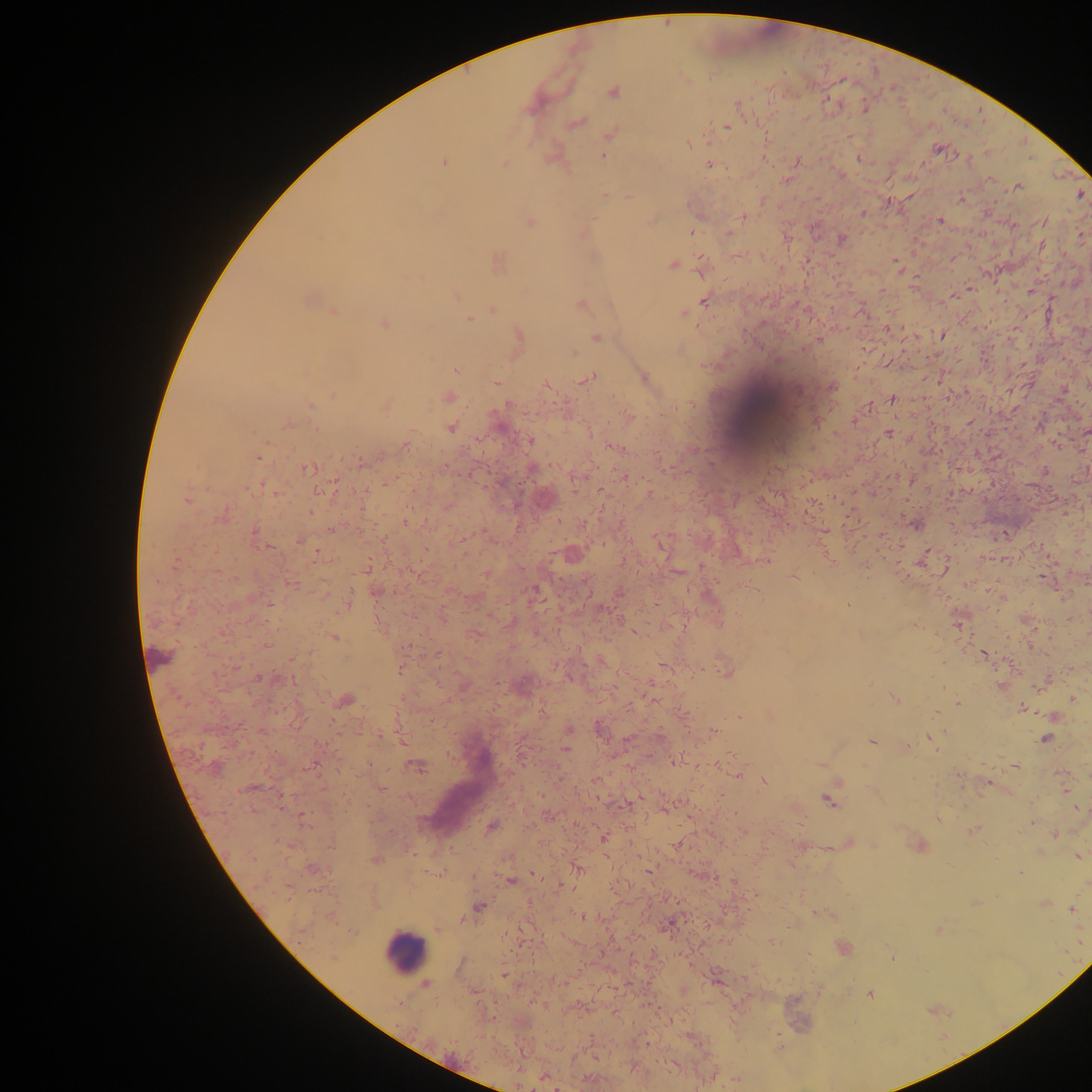

{
  "capture": "mobile-phone photograph through a microscope",
  "field_of_view": "single",
  "image_size": "1092×1092 pixels",
  "malaria_parasite_locations": "approximate centers as (x, y) in pixels: (612, 92), (738, 104), (577, 123), (726, 128), (611, 134), (689, 143), (938, 148), (602, 157), (797, 161), (444, 163), (709, 164), (1017, 187), (1081, 195), (605, 196), (629, 196), (742, 217), (940, 220), (529, 223), (691, 231), (729, 233), (841, 238), (1041, 245), (701, 259), (497, 261), (895, 261), (672, 266), (456, 296), (308, 300), (705, 300), (580, 305), (493, 309), (334, 313), (685, 314), (468, 319), (384, 324), (518, 335), (941, 335), (596, 337), (574, 353), (456, 370), (644, 378), (588, 379), (495, 383), (832, 388), (333, 394), (448, 397), (892, 400), (508, 403), (309, 405), (385, 405), (869, 406), (630, 417), (288, 424), (450, 429), (1087, 431), (889, 434), (529, 441), (1056, 444), (405, 445), (614, 447), (259, 457), (361, 463), (308, 469), (1044, 471), (622, 476), (912, 480), (260, 485), (650, 493), (187, 500), (310, 511), (220, 516), (406, 521), (916, 524), (332, 530), (254, 531), (661, 544), (269, 547), (573, 554), (764, 560), (366, 569), (794, 577), (291, 584), (534, 591), (708, 595), (347, 603), (847, 606), (334, 637), (984, 654), (400, 669), (726, 672), (259, 678), (292, 679), (894, 698), (1072, 699), (345, 701), (957, 703), (1022, 708), (739, 716), (1053, 716), (598, 727), (568, 730), (714, 732), (931, 737), (1045, 739), (871, 742), (566, 750), (677, 762), (1014, 765), (417, 766), (764, 782), (987, 784), (380, 788), (829, 801), (303, 818), (938, 819), (491, 826), (974, 832), (1054, 834), (603, 838), (849, 842), (330, 846), (920, 846), (1079, 856), (375, 860), (311, 867), (578, 868), (648, 869), (1020, 873), (510, 880), (733, 882), (1044, 903), (478, 906), (1071, 909), (581, 916), (462, 920), (773, 942), (843, 948), (892, 958), (504, 975), (426, 984), (870, 994), (736, 1080)",
  "preparation": "thick blood film",
  "country": "Ghana",
  "leukocyte_locations": "approximate centers as (x, y) in pixels: (762, 409), (159, 657), (405, 952)"
}